Assess for parasitized red blood cells.
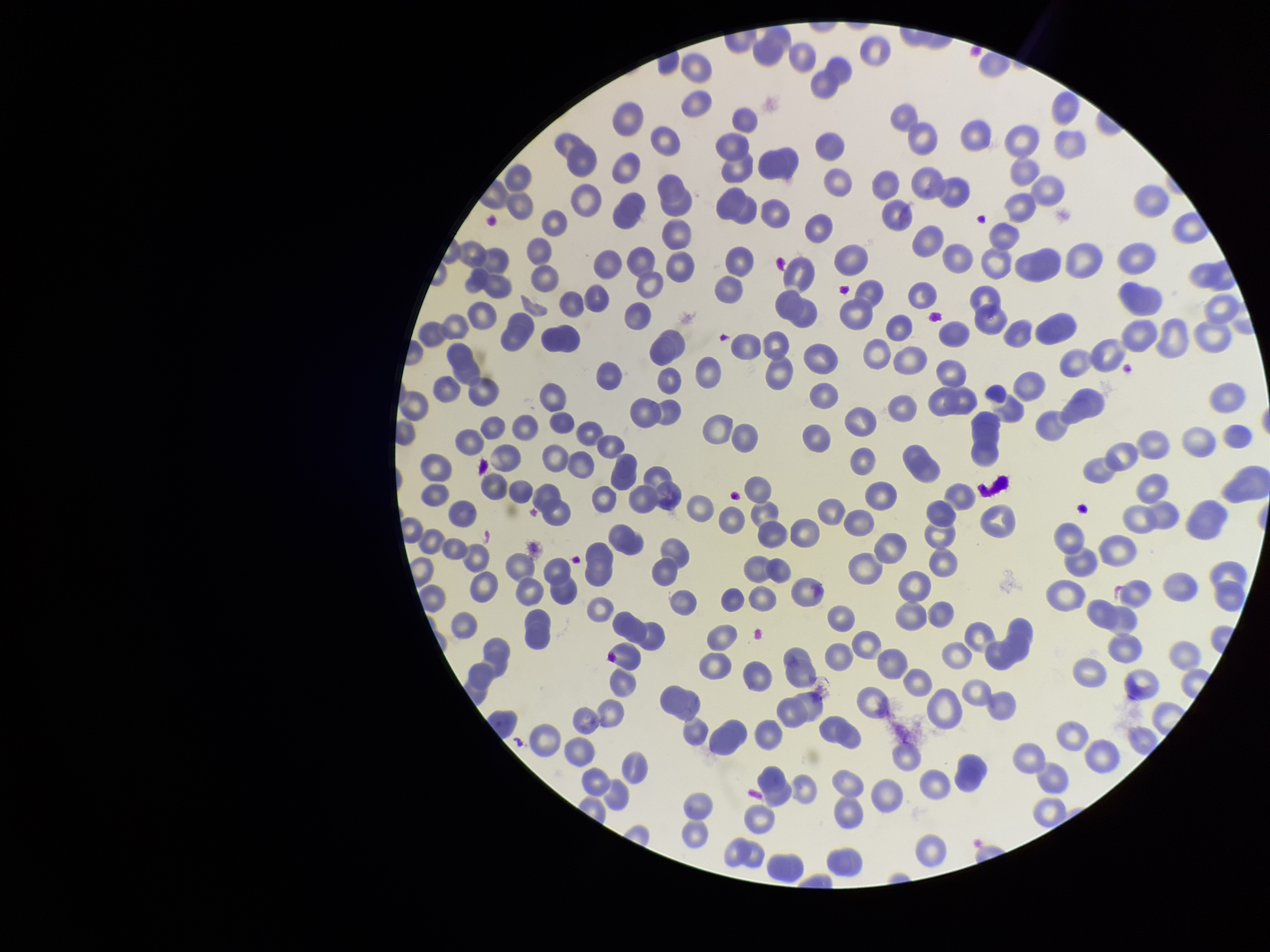
None seen.

capture = smartphone photograph through the microscope eyepiece
stain = Giemsa
preparation = thin
parasitized red blood cell count = 0
image size = 1270×952 pixels
species reported for this patient = Plasmodium vivax
patient malaria status = positive
red blood cell count = 234
field of view = one from this slide